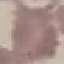 Result: no malaria parasites seen. Acquired by smartphone through the microscope eyepiece. Giemsa-stained preparation. Automatically extracted cell patch, resized to 64 × 64 pixels. Thin blood smear.